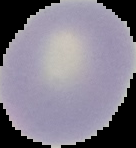 The area outside the segmented cell region is set to black. Image is 136×148 pixels. From a thin blood film. Malaria status: uninfected.